Report the malaria status of this cell.
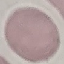

It is uninfected.

Summary:
  - Capture: smartphone through the microscope eyepiece
  - Preparation: thin smear
  - Image type: cell patch, automatically extracted from a larger field of view and resized to 64 × 64 pixels
  - Stain: Giemsa